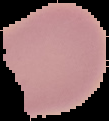
image_size: 109×121 pixels
preparation: thin blood film
image_type: segmented cell region with the area outside set to black
malaria_status: uninfected